Outline each Plasmodium malariae-infected red blood cell.
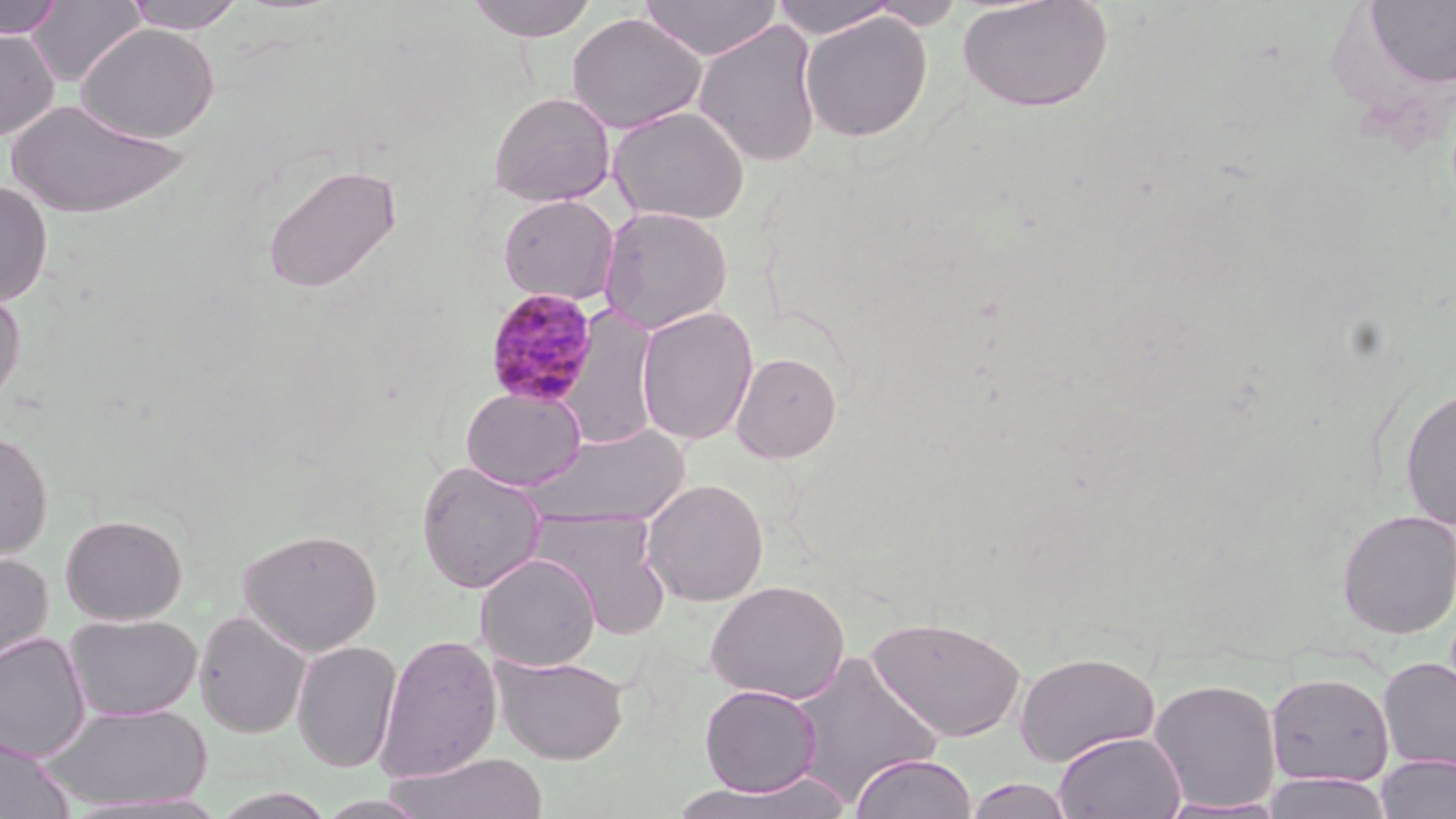
Approximate bounding boxes as [x1, y1, x2, y2] in pixels.
Plasmodium malariae-infected red blood cells: [483, 286, 600, 407].

Uninfected red blood cell locations: [0, 0, 65, 39], [25, 0, 147, 87], [121, 0, 247, 33], [463, 0, 600, 42], [638, 0, 782, 60], [957, 0, 1114, 113], [768, 1, 901, 39], [1358, 2, 1456, 89], [567, 12, 707, 134], [799, 12, 933, 142], [693, 21, 823, 167], [76, 23, 219, 143], [0, 28, 59, 141], [487, 91, 616, 207], [5, 98, 192, 219], [609, 105, 750, 225], [261, 163, 403, 294], [0, 179, 54, 307], [497, 193, 620, 306], [598, 206, 733, 334], [0, 285, 27, 409], [635, 306, 759, 446], [730, 351, 842, 463], [461, 386, 587, 491], [1399, 386, 1456, 531], [526, 424, 690, 528], [0, 428, 53, 560], [416, 460, 547, 593], [641, 478, 769, 606], [530, 509, 671, 638], [1336, 509, 1455, 638], [60, 514, 187, 625], [238, 527, 383, 656], [0, 550, 54, 671], [475, 553, 601, 671], [705, 579, 850, 704], [194, 609, 311, 738], [65, 613, 203, 722], [866, 615, 1026, 743], [0, 632, 92, 762], [375, 632, 502, 782], [292, 640, 402, 773], [1015, 650, 1160, 766], [785, 651, 945, 806], [491, 653, 630, 765], [1378, 656, 1456, 773], [1265, 672, 1395, 788], [1148, 678, 1283, 813], [699, 684, 822, 797], [41, 702, 212, 811], [1053, 731, 1187, 819], [0, 737, 75, 818], [384, 751, 549, 819], [850, 753, 977, 819], [1375, 754, 1456, 819], [1261, 773, 1396, 819], [678, 774, 853, 817], [964, 778, 1076, 819]. Slide-level diagnosis: Plasmodium malariae. One field of a larger specimen. Image is 1456×819 pixels. May-Grünwald-Giemsa stain. Light microscopy. Captured at 1000x magnification. Thin blood film.